Classify this cell by malaria status.
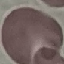

It is uninfected.

Summary:
  - Image type: cell patch, automatically extracted from a larger field of view and resized to 64 × 64 pixels
  - Preparation: thin smear
  - Capture: smartphone camera at the microscope eyepiece
  - Stain: Giemsa